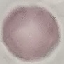

malaria status = uninfected
preparation = thin blood film
capture = smartphone through the microscope eyepiece
stain = Giemsa
image type = cell patch, automatically extracted from a larger field of view and resized to 64 × 64 pixels